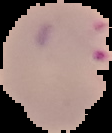

Image is 112×133 pixels. From a thin blood film. Result: malaria parasites detected. Segmented cell region on a black background.